Identify the blood parasite species.
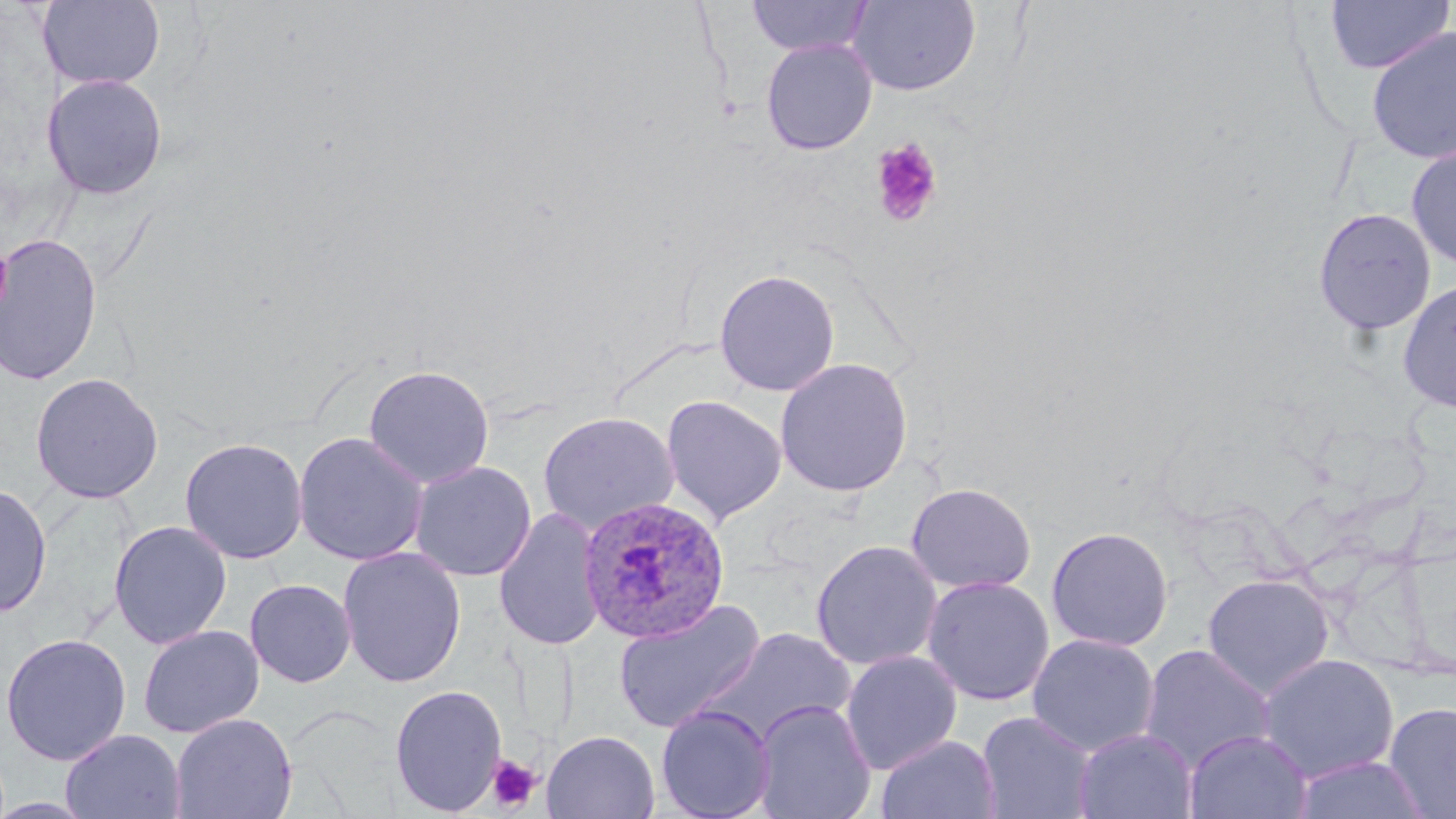

Plasmodium ovale.

Summary:
  - Coordinate format: approximate bounding boxes as (x1,y1)-(x2,y2) corner pairs in pixels
  - Uninfected red blood cell locations: (38,0)-(165,91), (746,0)-(874,57), (1324,0)-(1453,75), (846,1)-(981,96), (1365,26)-(1456,165), (760,38)-(878,155), (41,74)-(168,200), (1405,144)-(1456,271), (1313,207)-(1437,337), (0,234)-(103,387), (714,268)-(840,397), (1397,279)-(1456,414), (775,357)-(913,496), (363,365)-(494,489), (30,372)-(164,504), (660,394)-(787,526), (538,411)-(679,536), (293,431)-(429,566), (180,437)-(308,564), (409,460)-(536,581), (906,482)-(1036,594), (0,483)-(52,618), (494,507)-(605,652), (109,520)-(232,650), (1046,526)-(1173,651), (810,540)-(942,671), (337,547)-(466,688), (1202,574)-(1335,698), (922,576)-(1055,706), (245,579)-(356,687), (614,599)-(765,734), (138,624)-(264,738), (699,628)-(857,749), (0,633)-(131,765), (1026,634)-(1159,756), (1139,644)-(1275,773), (841,651)-(962,774), (1257,653)-(1399,782), (389,684)-(507,816), (752,699)-(877,819), (1384,702)-(1456,819), (656,705)-(776,819), (976,711)-(1098,819), (170,712)-(297,819), (1074,728)-(1198,818), (60,729)-(186,818), (1184,729)-(1312,819), (541,730)-(660,819), (876,735)-(1001,819), (1289,755)-(1434,819)
  - Platelet locations: (870,139)-(943,227), (0,242)-(12,317), (487,755)-(542,812)
  - Plasmodium ovale-infected red blood cell locations: (577,495)-(730,643)
  - Field of view: one of a larger specimen
  - Modality: light microscopy
  - Image size: 1456×819 pixels
  - Stain: May-Grünwald-Giemsa
  - Preparation: thin blood smear
  - Magnification: 1000x